Name the blood parasite species.
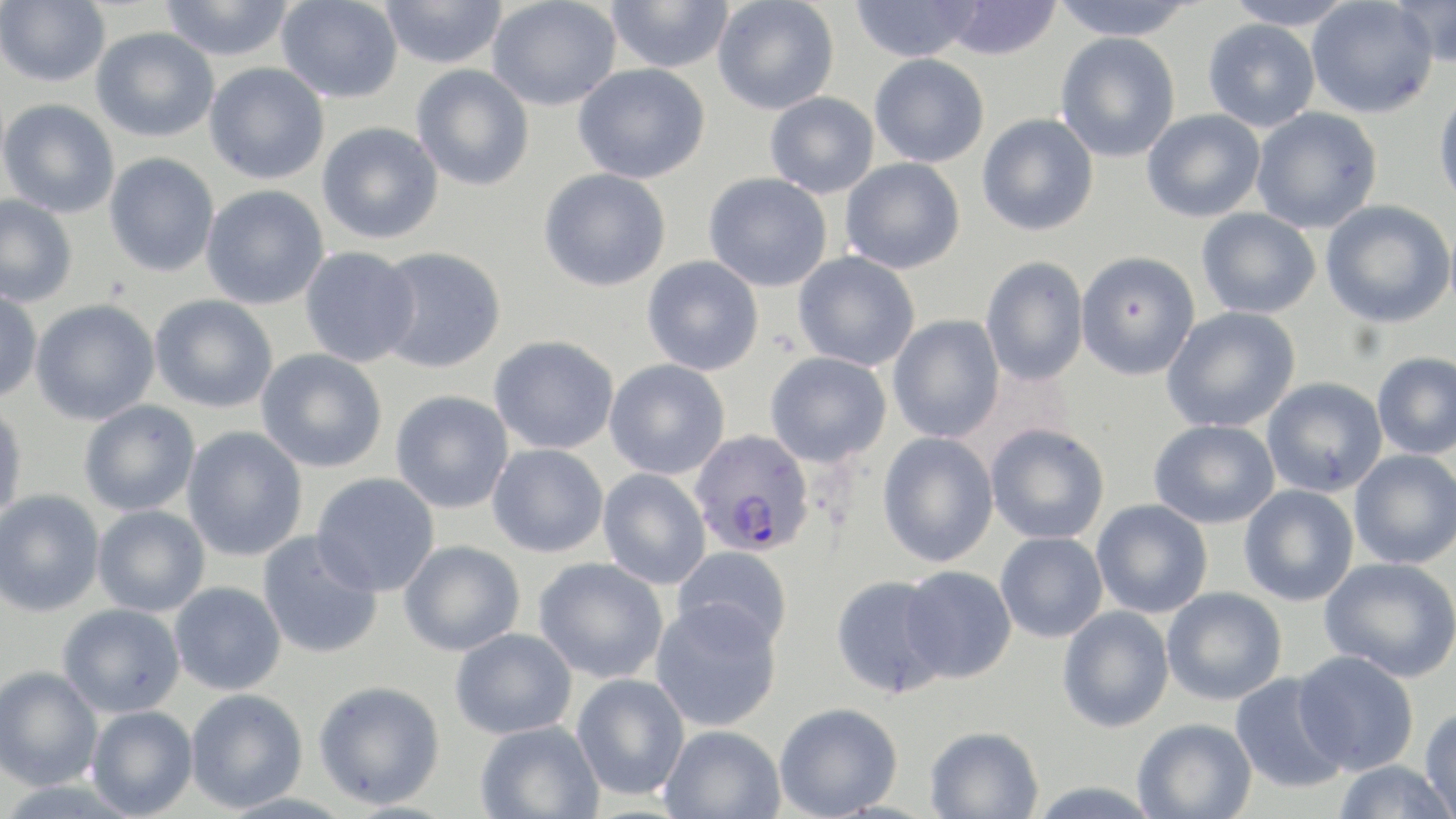

Plasmodium falciparum.

Summary:
  - Coordinate format: approximate bounding boxes as (x1,y1)-(x2,y2) corner pairs in pixels
  - Plasmodium falciparum-infected red blood cell locations: (689,429)-(815,557)
  - Uninfected red blood cell locations: (0,0)-(110,87), (158,0)-(295,62), (487,0)-(621,111), (606,0)-(734,73), (712,0)-(840,115), (850,0)-(981,63), (1048,0)-(1199,40), (1222,0)-(1358,30), (1306,0)-(1438,118), (1392,0)-(1456,67), (276,1)-(403,103), (380,1)-(508,69), (938,1)-(1062,60), (1202,18)-(1321,132), (91,27)-(219,142), (1055,32)-(1181,162), (869,54)-(990,167), (204,62)-(330,184), (573,63)-(710,184), (411,65)-(534,191), (1433,87)-(1456,213), (765,92)-(879,198), (0,98)-(120,218), (1251,107)-(1383,234), (1142,109)-(1266,222), (977,113)-(1099,236), (317,122)-(443,245), (104,152)-(219,277), (840,158)-(965,274), (539,168)-(671,292), (703,172)-(832,292), (201,185)-(329,309), (0,194)-(78,308), (1321,200)-(1455,328), (1196,208)-(1322,319), (299,246)-(420,367), (374,247)-(506,374), (793,251)-(920,371), (1075,251)-(1200,380), (642,255)-(764,376), (980,256)-(1089,386), (0,289)-(42,403), (150,294)-(277,413), (30,298)-(160,425), (1161,307)-(1300,433), (888,315)-(1005,443), (489,335)-(619,455), (256,349)-(387,473), (764,352)-(892,467), (1371,352)-(1456,460), (604,359)-(729,480), (1261,377)-(1387,497), (390,389)-(513,514), (79,400)-(200,516), (0,401)-(27,523), (1149,419)-(1280,529), (985,423)-(1110,544), (182,426)-(308,562), (877,432)-(999,567), (487,443)-(608,558), (1349,449)-(1456,570), (598,468)-(711,589), (311,472)-(440,597), (1238,485)-(1359,606), (0,489)-(105,617), (1091,499)-(1213,618), (92,505)-(210,617), (257,531)-(382,659), (995,532)-(1107,643), (399,540)-(525,656), (672,545)-(793,650), (533,557)-(668,683), (1319,557)-(1456,683), (900,565)-(1017,683), (830,575)-(952,699), (169,582)-(286,696), (1161,587)-(1287,706), (650,600)-(782,731), (57,604)-(185,718), (1057,607)-(1175,732), (450,627)-(577,740), (1294,650)-(1420,776), (0,665)-(103,790), (1230,672)-(1349,794), (572,673)-(690,800), (313,680)-(445,809), (185,688)-(309,813), (774,702)-(903,819), (86,706)-(198,818), (1420,706)-(1456,819), (1133,718)-(1257,819), (475,721)-(603,819), (659,724)-(786,819), (924,725)-(1044,818), (1332,760)-(1454,818), (1026,781)-(1165,818)
  - Preparation: thin blood film
  - Modality: light microscopy
  - Magnification: 1000x
  - Image size: 1456×819 pixels
  - Stain: May-Grünwald-Giemsa
  - Field of view: single